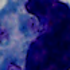
modality: micrograph
magnification: 1000x
identification: leukocyte